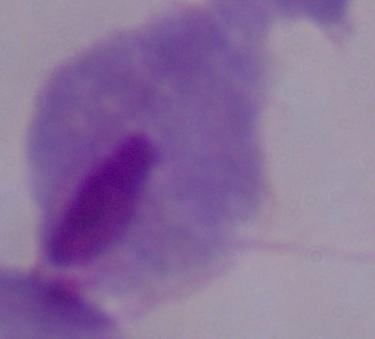
Summary:
  - Modality: photomicrograph
  - Magnification: 1000x
  - Identification: trichomonad